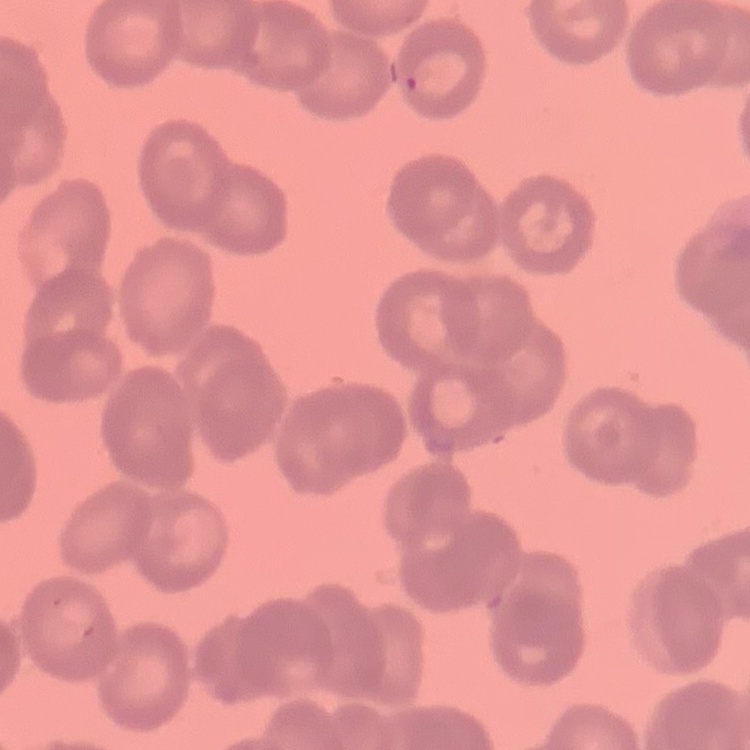

The erythrocytes exhibit rouleaux formation. Thin blood film. Field's or Giemsa stain. One tile cut from a larger photomicrograph.